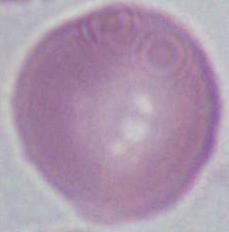

{
  "magnification": "1000x",
  "identification": "red blood cell",
  "modality": "photomicrograph"
}